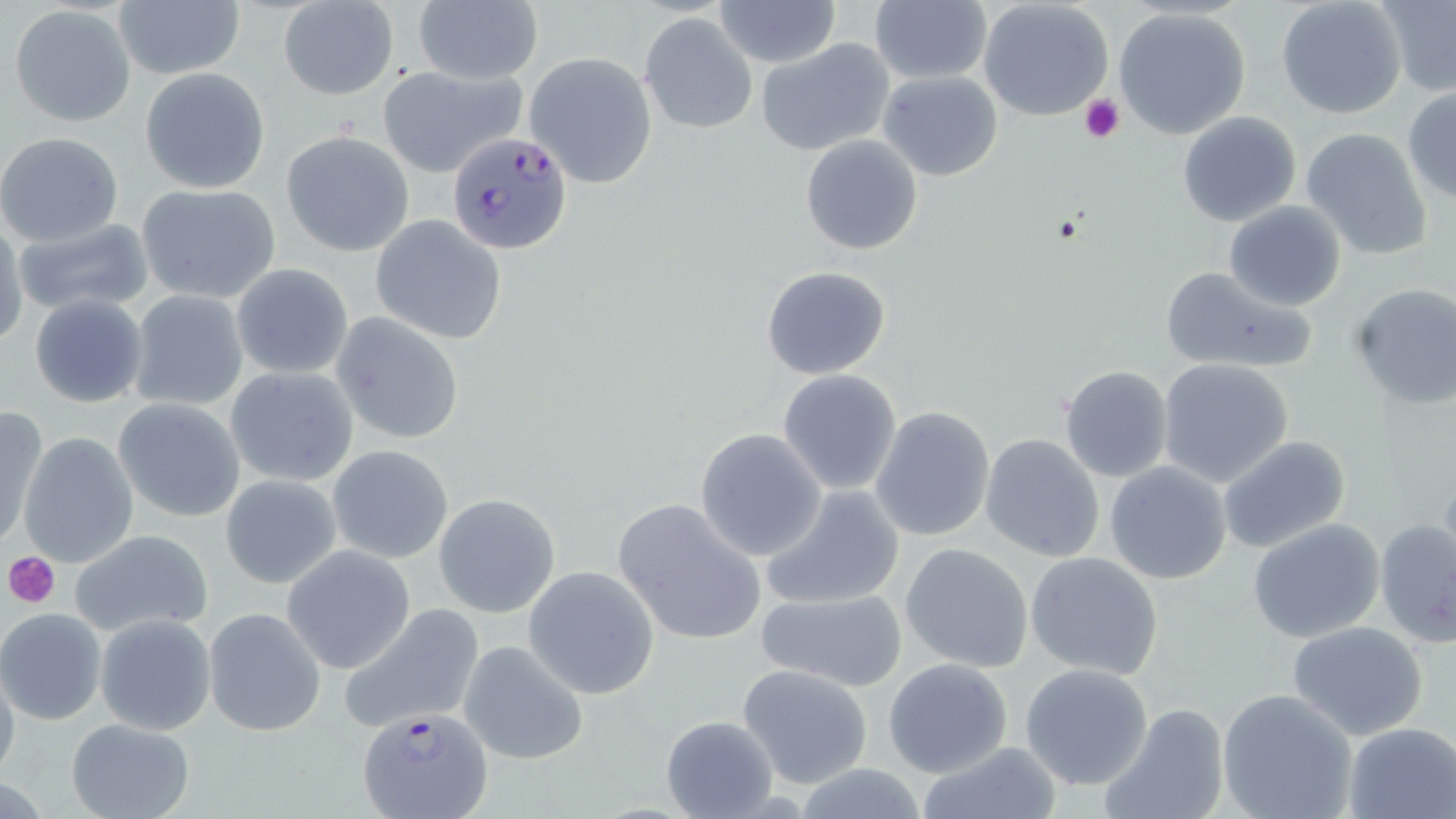
Summary:
  - Coordinate format: approximate bounding boxes as [x1, y1, x2, y2] in pixels
  - Plasmodium falciparum-infected red blood cell locations: [446, 130, 573, 255], [359, 709, 494, 819]
  - Uninfected red blood cell locations: [412, 0, 542, 86], [713, 0, 840, 69], [978, 0, 1114, 120], [1276, 0, 1406, 118], [1377, 0, 1456, 95], [113, 1, 244, 81], [277, 2, 399, 100], [868, 2, 992, 85], [9, 5, 137, 127], [1113, 5, 1252, 140], [640, 12, 759, 135], [757, 38, 894, 157], [523, 51, 658, 189], [377, 65, 525, 178], [141, 68, 271, 193], [878, 71, 1003, 181], [1402, 87, 1456, 203], [1176, 111, 1303, 227], [1301, 126, 1434, 259], [281, 130, 414, 257], [0, 132, 125, 246], [801, 134, 923, 255], [137, 183, 280, 304], [1224, 201, 1347, 311], [370, 216, 507, 345], [13, 217, 154, 315], [0, 222, 26, 348], [231, 263, 353, 380], [760, 265, 892, 381], [1158, 266, 1320, 376], [1349, 281, 1456, 410], [126, 290, 249, 411], [28, 293, 149, 408], [330, 312, 466, 445], [1157, 359, 1292, 487], [1059, 365, 1174, 482], [226, 366, 359, 488], [777, 369, 903, 495], [113, 398, 246, 522], [0, 406, 48, 552], [871, 406, 997, 543], [695, 430, 826, 560], [18, 432, 140, 567], [980, 434, 1104, 563], [1217, 435, 1352, 554], [326, 445, 453, 564], [639, 453, 817, 619], [1104, 462, 1233, 585], [220, 474, 342, 589], [759, 484, 905, 611], [433, 493, 561, 618], [613, 497, 767, 646], [1374, 517, 1456, 649], [1248, 519, 1385, 643], [67, 528, 214, 641], [900, 543, 1032, 674], [282, 546, 415, 674], [1025, 552, 1165, 680], [522, 565, 660, 699], [753, 586, 909, 692], [338, 603, 485, 733], [203, 607, 327, 736], [0, 608, 106, 724], [95, 614, 215, 735], [1287, 621, 1429, 739], [458, 639, 589, 764], [0, 655, 21, 787], [883, 658, 1013, 777], [735, 662, 876, 788], [1019, 663, 1154, 790], [1216, 688, 1358, 819], [1096, 702, 1231, 819], [659, 715, 779, 816], [66, 718, 195, 819], [1342, 722, 1455, 819], [914, 740, 1064, 819]
  - Platelet locations: [1078, 93, 1125, 142], [5, 552, 61, 611]
  - Slide-level diagnosis: Plasmodium falciparum
  - Field of view: single
  - Stain: May-Grünwald-Giemsa
  - Image size: 1456×819 pixels
  - Preparation: thin blood film
  - Modality: optical microscopy
  - Magnification: 1000x